Name the parasite shown.
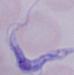

This is a trypanosome.

Summary:
  - Magnification: 1000x
  - Modality: micrograph